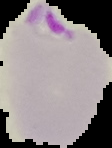

The area outside the segmented cell region is set to black. From a thin blood film. Result: malaria parasites detected. Image is 112×148 pixels.